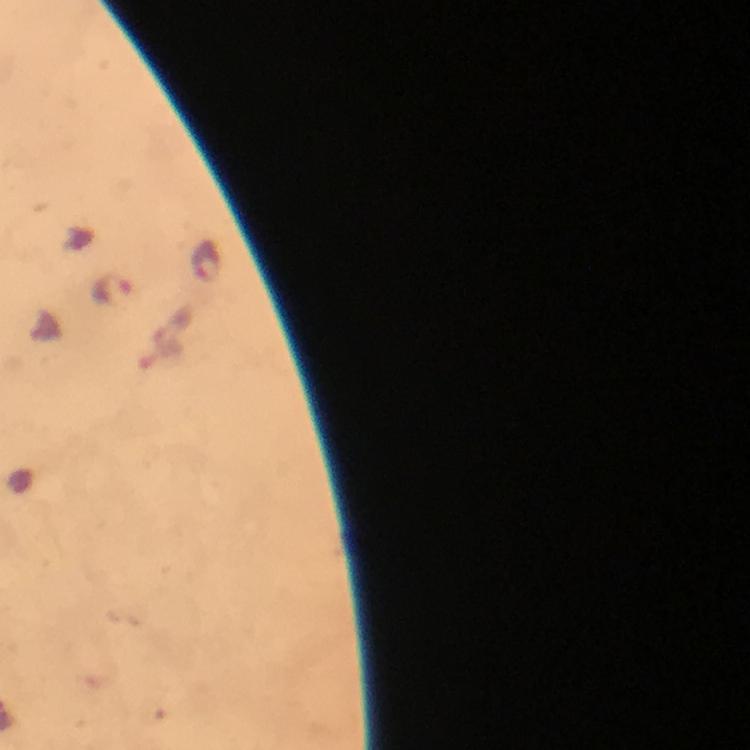 Approximate object centers, in pixels from the top-left corner. Plasmodium parasite locations: (x=210, y=260), (x=114, y=288). At 100x magnification. From a diagnostic examination for malaria. Giemsa stain. Immersion oil applied. Image is 750×750 pixels. A crop from one field of view. Thick smear. Photographed with a smartphone mounted on the microscope.